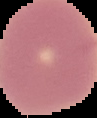
Cell region segmented out of the field of view; the surrounding area is masked to black. Result: no Plasmodium parasites detected. Image is 97×118 pixels. From a thin blood smear.